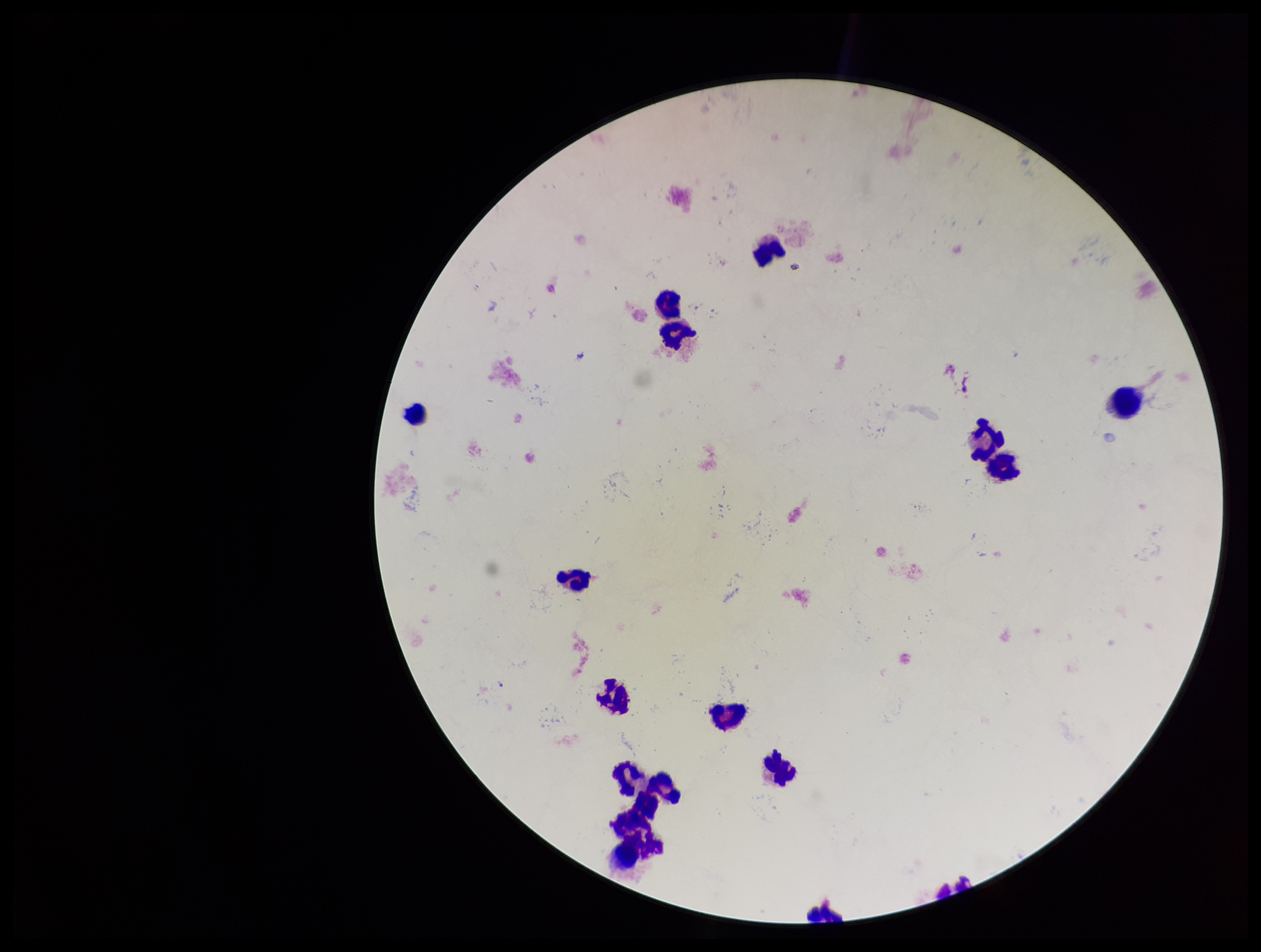

image size = 1261×952 pixels
leukocyte count = 16
capture = smartphone photograph through the microscope eyepiece
Plasmodium parasites = none detected
patient malaria status = negative
preparation = thick
field of view = one from this slide
parasite count = 0
stain = Giemsa